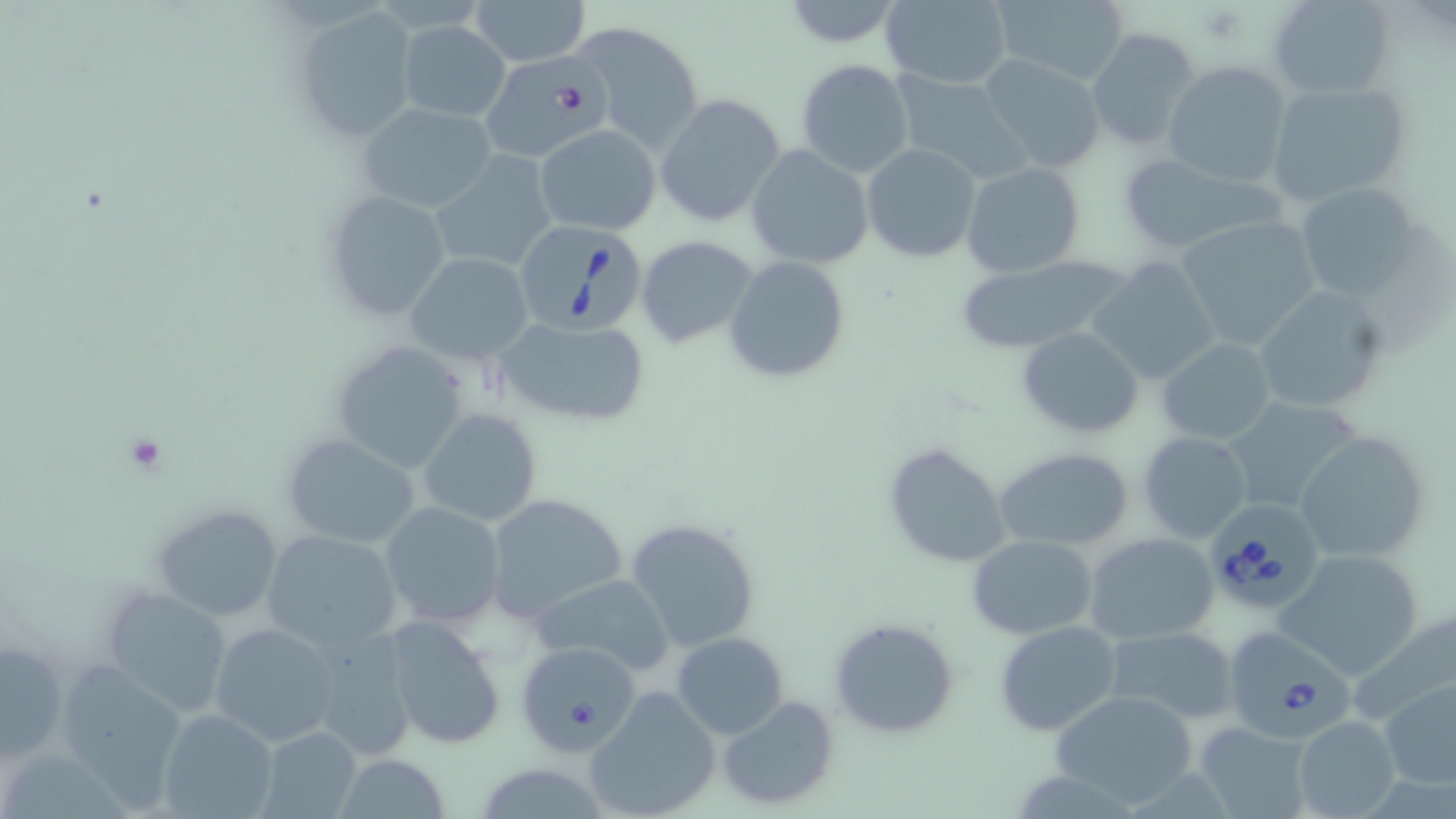 Approximate bounding boxes as named x1/y1/x2/y2 corners in pixels. Platelet locations: (x1=119, y1=432, x2=169, y2=475). Babesia divergens-infected red blood cell locations: (x1=519, y1=219, x2=650, y2=334), (x1=1205, y1=500, x2=1325, y2=610), (x1=1231, y1=630, x2=1355, y2=736). Uninfected red blood cell locations: (x1=467, y1=0, x2=593, y2=67), (x1=777, y1=0, x2=908, y2=50), (x1=879, y1=0, x2=1013, y2=90), (x1=990, y1=0, x2=1130, y2=85), (x1=1268, y1=0, x2=1394, y2=98), (x1=292, y1=9, x2=420, y2=146), (x1=397, y1=19, x2=511, y2=122), (x1=569, y1=20, x2=705, y2=156), (x1=1087, y1=27, x2=1202, y2=152), (x1=978, y1=52, x2=1108, y2=176), (x1=481, y1=53, x2=613, y2=162), (x1=795, y1=58, x2=915, y2=178), (x1=1162, y1=60, x2=1291, y2=189), (x1=890, y1=71, x2=1031, y2=184), (x1=1264, y1=80, x2=1410, y2=207), (x1=654, y1=93, x2=786, y2=229), (x1=356, y1=102, x2=498, y2=215), (x1=535, y1=124, x2=661, y2=235), (x1=862, y1=143, x2=981, y2=262), (x1=746, y1=145, x2=873, y2=268), (x1=429, y1=152, x2=558, y2=275), (x1=1116, y1=155, x2=1277, y2=255), (x1=962, y1=162, x2=1084, y2=279), (x1=1293, y1=179, x2=1429, y2=301), (x1=322, y1=189, x2=454, y2=322), (x1=1175, y1=215, x2=1323, y2=350), (x1=636, y1=235, x2=760, y2=348), (x1=405, y1=253, x2=534, y2=363), (x1=724, y1=256, x2=851, y2=386), (x1=948, y1=256, x2=1138, y2=357), (x1=1087, y1=257, x2=1220, y2=386), (x1=1251, y1=283, x2=1392, y2=416), (x1=495, y1=316, x2=653, y2=428), (x1=1016, y1=326, x2=1144, y2=439), (x1=330, y1=339, x2=470, y2=474), (x1=1157, y1=339, x2=1276, y2=443), (x1=1221, y1=397, x2=1363, y2=516), (x1=418, y1=408, x2=544, y2=528), (x1=1294, y1=428, x2=1432, y2=562), (x1=1138, y1=432, x2=1251, y2=542), (x1=281, y1=434, x2=421, y2=550), (x1=882, y1=440, x2=1013, y2=569), (x1=995, y1=448, x2=1136, y2=549), (x1=483, y1=493, x2=628, y2=625), (x1=378, y1=501, x2=509, y2=630), (x1=150, y1=504, x2=284, y2=623), (x1=623, y1=517, x2=763, y2=653), (x1=261, y1=529, x2=403, y2=654), (x1=1084, y1=532, x2=1220, y2=643), (x1=967, y1=535, x2=1097, y2=639), (x1=1273, y1=547, x2=1428, y2=679), (x1=527, y1=573, x2=676, y2=676), (x1=100, y1=585, x2=234, y2=716), (x1=384, y1=614, x2=506, y2=747), (x1=829, y1=615, x2=960, y2=740), (x1=208, y1=621, x2=339, y2=746), (x1=994, y1=621, x2=1123, y2=737), (x1=1103, y1=626, x2=1240, y2=724), (x1=306, y1=627, x2=418, y2=763), (x1=672, y1=632, x2=789, y2=739), (x1=0, y1=637, x2=67, y2=760), (x1=516, y1=644, x2=644, y2=750), (x1=52, y1=659, x2=189, y2=804), (x1=1379, y1=677, x2=1456, y2=790), (x1=593, y1=685, x2=733, y2=817), (x1=1048, y1=691, x2=1199, y2=806), (x1=718, y1=694, x2=840, y2=811), (x1=156, y1=708, x2=279, y2=819), (x1=1293, y1=715, x2=1402, y2=819), (x1=1192, y1=720, x2=1312, y2=818), (x1=258, y1=726, x2=362, y2=818), (x1=328, y1=755, x2=456, y2=817), (x1=484, y1=763, x2=610, y2=819). Slide-level diagnosis: Babesia divergens. 1000x magnification. Light microscopy. Image is 1456×819 pixels. Single field of view. Thin blood smear. May-Grünwald-Giemsa-stained preparation.